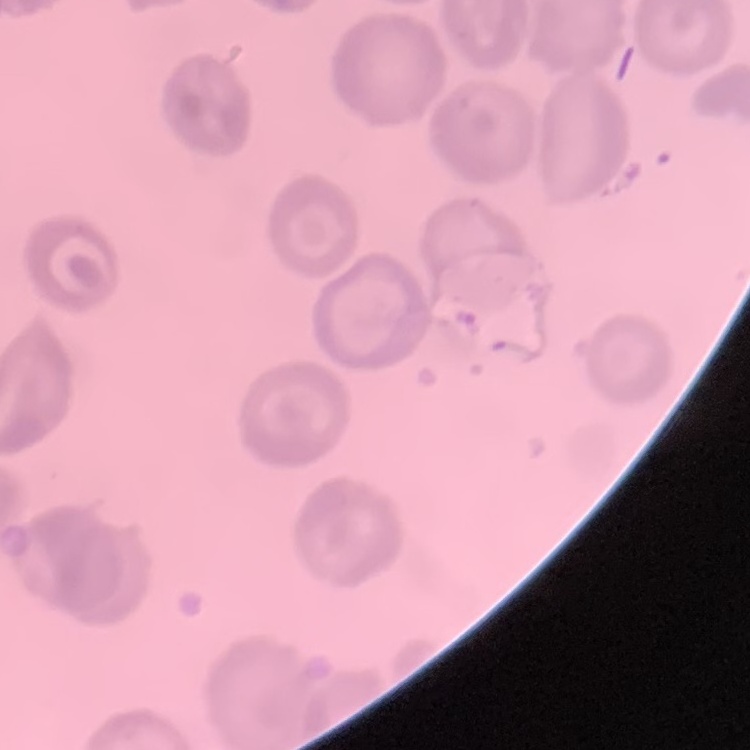 The erythrocytes show no rouleaux formation. One tile cut from a larger photomicrograph. Field's or Giemsa stain. Thin blood film.